Report the malaria status of this cell.
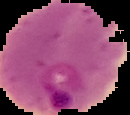

It is parasitized.

From a thin blood smear. Image is 130×115 pixels. The area outside the segmented cell region is set to black.